Assess this cell for malaria.
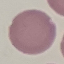

Uninfected.

Thin smear of blood. Giemsa-stained preparation. Acquired by smartphone through the microscope eyepiece. Automatically extracted cell patch, resized to 64 × 64 pixels.